State which parasite is depicted.
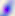
Toxoplasma gondii.

400x magnification. Photomicrograph.